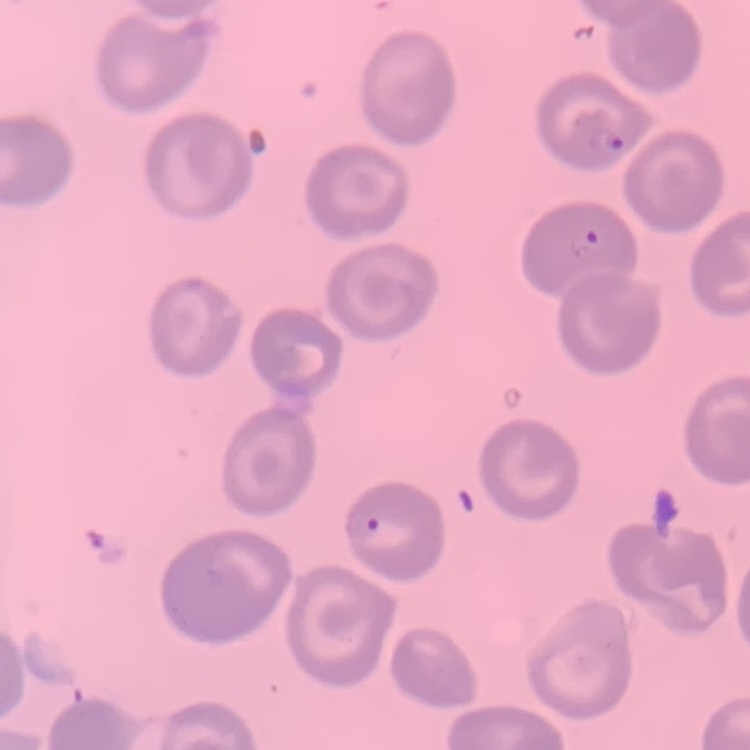 The red blood cells show no rouleaux formation. One tile cut from a larger photomicrograph. Field's or Giemsa stain. Thin blood film.